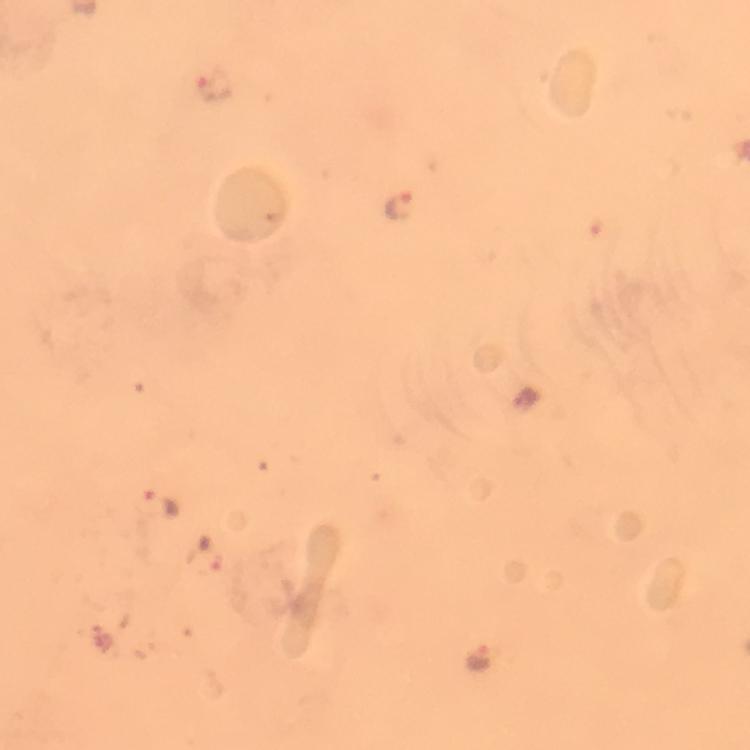
Approximate centers as [x, y] in pixels.
Summary:
  - Plasmodium parasite locations: [216, 85], [401, 206], [526, 401], [162, 506], [477, 660]
  - Capture: smartphone camera through the microscope
  - Context: from a malaria diagnostic workup
  - Image size: 750×750 pixels
  - Stain: Giemsa
  - Preparation: thick smear
  - Magnification: 100x
  - Cropped from: a single field of view
  - Immersion oil: used